Classify this cell by malaria status.
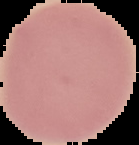

It is uninfected.

Image is 139×145 pixels. From a thin blood film. The area outside the segmented cell region is set to black.